Assess the morphology of the erythrocytes.
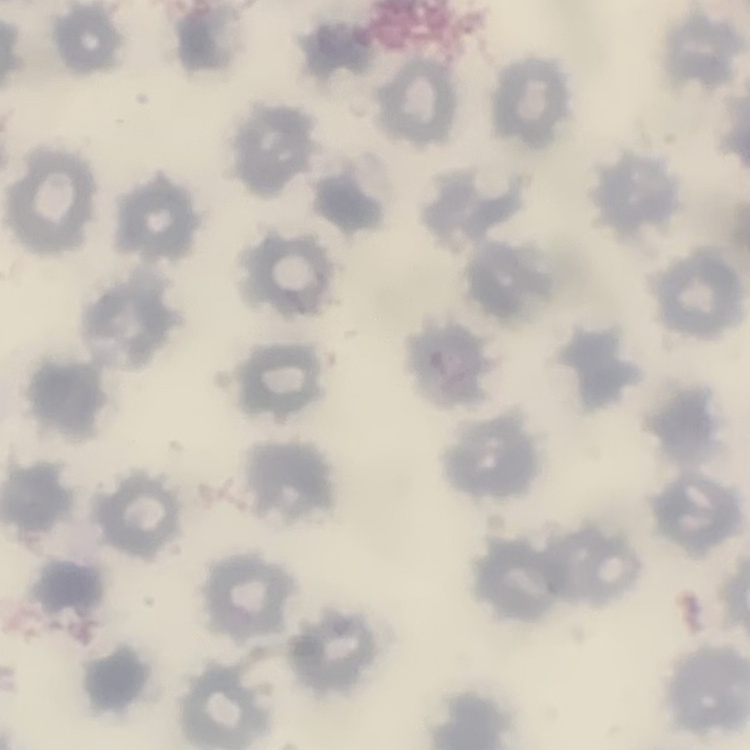

No rouleaux formation.

Thin peripheral smear. One tile cut from a larger photomicrograph. Stained with either Field's or Giemsa.